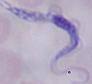
Summary:
  - Modality: photomicrograph
  - Magnification: 1000x
  - Identification: trypanosome